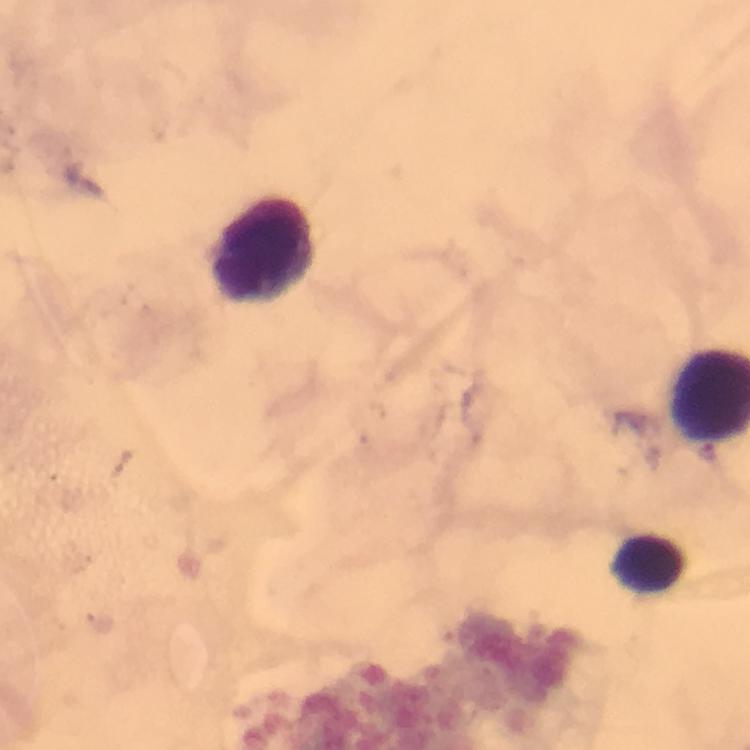

Approximate object centers, in pixels from the top-left corner.
Summary:
  - Leukocyte locations: (x=267, y=248), (x=648, y=563)
  - Malaria parasite locations: (x=708, y=452)
  - Stain: Giemsa
  - Cropped from: a single field of view
  - Capture: smartphone mounted on the microscope
  - Image size: 750×750 pixels
  - Immersion oil: applied
  - Context: from a malaria diagnostic workup
  - Preparation: thick blood film
  - Magnification: 100x